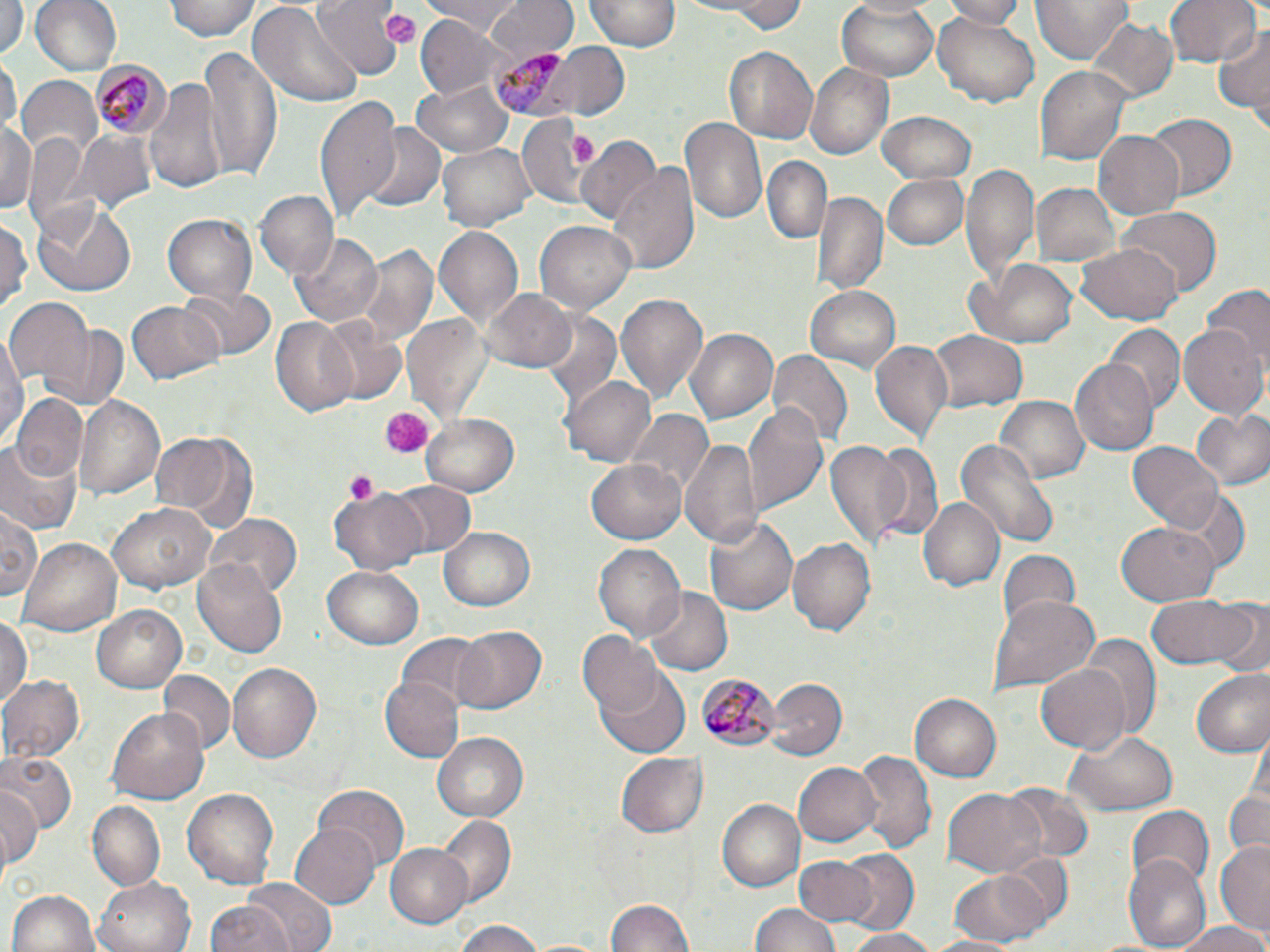
Summary:
  - Coordinate format: approximate bounding boxes as [x1, y1, x2, y2] in pixels
  - Uninfected red blood cell locations: [28, 0, 122, 79], [167, 0, 262, 41], [312, 0, 404, 82], [416, 0, 527, 29], [486, 0, 576, 65], [587, 0, 682, 51], [693, 0, 809, 33], [945, 0, 1029, 26], [1032, 0, 1136, 64], [1165, 0, 1260, 71], [0, 1, 24, 58], [247, 2, 365, 110], [836, 2, 942, 81], [933, 9, 1040, 106], [414, 17, 509, 97], [1085, 17, 1178, 104], [1216, 23, 1269, 121], [533, 44, 631, 120], [199, 45, 280, 181], [723, 46, 817, 145], [2, 53, 20, 141], [805, 62, 892, 159], [1036, 66, 1134, 167], [144, 76, 228, 195], [13, 77, 101, 162], [413, 79, 512, 154], [316, 93, 403, 221], [878, 111, 977, 183], [1148, 113, 1236, 199], [517, 115, 593, 209], [680, 116, 768, 229], [0, 121, 37, 216], [360, 122, 447, 213], [2, 125, 77, 230], [75, 131, 156, 217], [1092, 131, 1183, 217], [577, 137, 661, 229], [435, 141, 533, 231], [763, 156, 830, 244], [610, 161, 700, 279], [963, 161, 1036, 287], [883, 173, 969, 250], [1030, 181, 1120, 270], [815, 191, 886, 297], [254, 192, 338, 280], [32, 199, 137, 297], [1116, 208, 1220, 297], [163, 215, 256, 301], [0, 217, 30, 311], [534, 221, 636, 312], [434, 226, 525, 332], [291, 233, 383, 327], [350, 243, 440, 348], [1078, 245, 1181, 324], [967, 261, 1078, 347], [1200, 285, 1270, 372], [805, 286, 902, 371], [179, 287, 276, 363], [482, 287, 579, 373], [614, 293, 707, 404], [6, 298, 94, 390], [127, 300, 224, 385], [403, 312, 490, 427], [539, 313, 622, 411], [313, 314, 411, 408], [271, 319, 359, 415], [41, 321, 129, 412], [1108, 323, 1182, 411], [1180, 323, 1268, 419], [684, 326, 781, 425], [1, 329, 27, 452], [927, 331, 1026, 409], [869, 340, 954, 444], [769, 350, 851, 446], [1070, 358, 1159, 456], [563, 375, 657, 468], [13, 393, 88, 484], [72, 393, 167, 502], [993, 396, 1089, 484], [744, 403, 830, 516], [1192, 408, 1270, 490], [627, 411, 715, 503], [419, 413, 521, 497], [149, 427, 257, 531], [823, 436, 912, 552], [957, 436, 1059, 546], [679, 438, 762, 548], [0, 440, 81, 534], [1127, 441, 1223, 530], [871, 443, 945, 540], [585, 456, 688, 544], [385, 480, 476, 560], [1170, 485, 1250, 570], [330, 487, 428, 575], [917, 497, 1005, 593], [108, 502, 216, 593], [2, 504, 42, 604], [706, 512, 799, 618], [204, 513, 305, 597], [1117, 520, 1220, 604], [440, 527, 534, 612], [786, 533, 877, 634], [24, 538, 121, 635], [593, 543, 686, 641], [995, 549, 1082, 633], [195, 558, 287, 659], [324, 565, 424, 648], [643, 586, 731, 677], [988, 594, 1099, 696], [1145, 596, 1250, 668], [1210, 601, 1270, 680], [90, 604, 187, 695], [0, 613, 31, 706], [451, 624, 547, 716], [580, 630, 663, 718], [395, 631, 494, 712], [1084, 633, 1160, 736], [1035, 661, 1132, 755], [226, 662, 324, 765], [593, 662, 691, 760], [1190, 668, 1270, 759], [158, 670, 235, 755], [1, 674, 85, 762], [383, 676, 464, 760], [767, 679, 844, 761], [910, 693, 1002, 783], [105, 705, 210, 807], [1062, 729, 1179, 814], [433, 732, 529, 823], [2, 750, 74, 833], [855, 750, 936, 856], [617, 752, 708, 834], [793, 762, 881, 847], [1, 785, 41, 869], [313, 785, 408, 865], [181, 788, 280, 889], [1003, 788, 1094, 862], [1222, 788, 1268, 861], [943, 789, 1044, 877], [719, 799, 803, 891], [89, 802, 165, 888], [1126, 805, 1214, 887], [438, 815, 517, 909], [291, 821, 381, 909], [1216, 841, 1270, 935], [386, 843, 474, 927], [1123, 850, 1211, 952], [837, 851, 920, 937], [997, 851, 1076, 931], [794, 857, 876, 928], [946, 866, 1055, 945], [93, 876, 195, 952], [239, 878, 338, 952], [6, 889, 101, 952], [605, 900, 696, 952], [204, 902, 292, 952], [752, 902, 842, 952], [452, 922, 550, 952], [1171, 922, 1270, 952], [845, 928, 944, 952], [920, 935, 1019, 952]
  - Plasmodium malariae-infected red blood cell locations: [487, 45, 581, 118], [91, 60, 170, 137], [696, 672, 778, 751]
  - Platelet locations: [378, 9, 421, 44], [570, 136, 595, 164], [378, 406, 429, 460], [344, 469, 379, 505]
  - Slide-level diagnosis: Plasmodium malariae
  - Magnification: 1000x
  - Image size: 1270×952 pixels
  - Preparation: thin blood smear
  - Modality: optical microscopy
  - Stain: May-Grünwald-Giemsa
  - Field of view: single